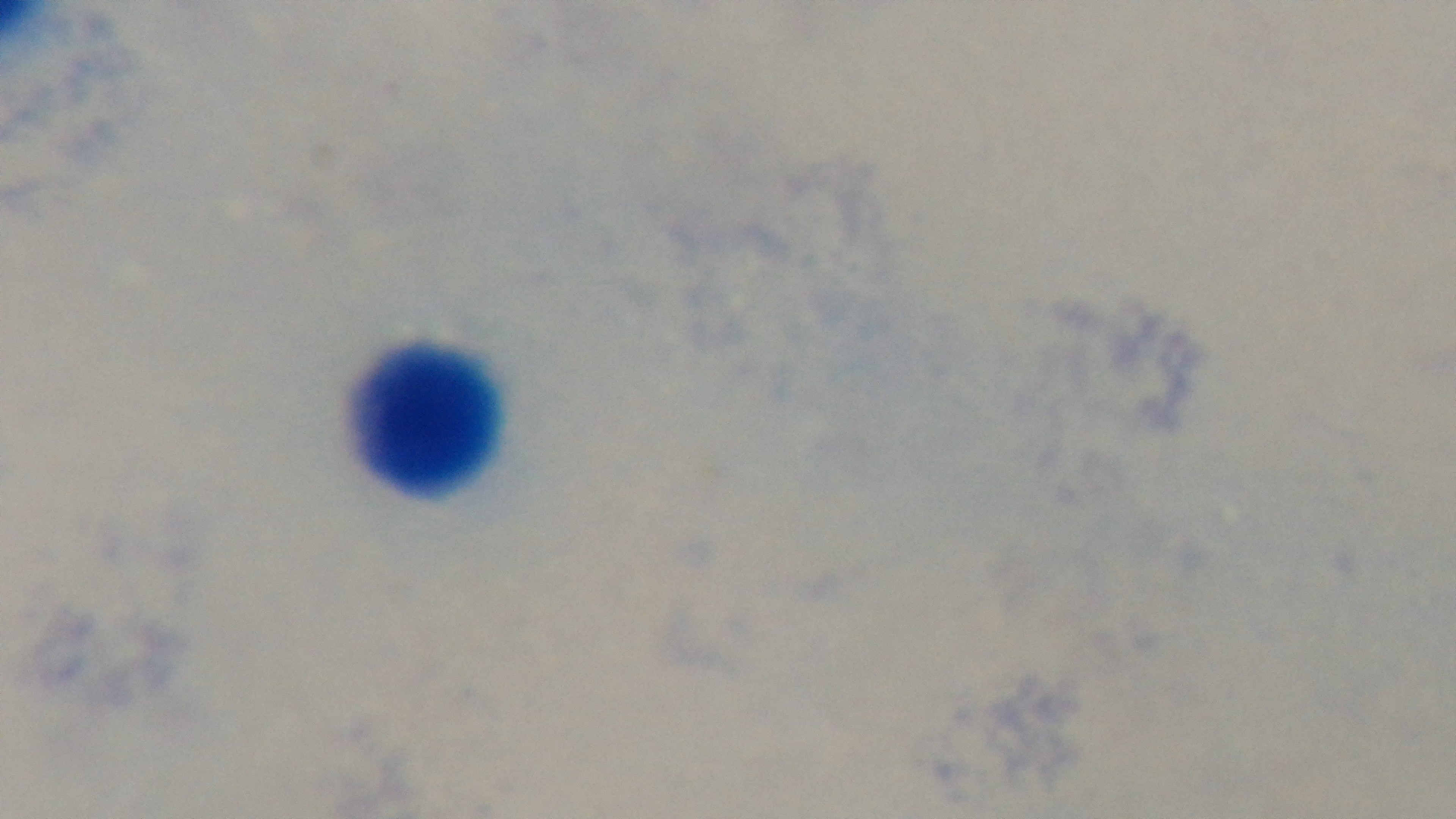
Summary:
  - Modality: light microscopy
  - Malaria status: uninfected
  - Objective: 100x oil immersion
  - Field of view: single
  - Capture: mounted 4K digital camera
  - Preparation: thick smear
  - Stain: Giemsa